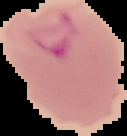
Summary:
  - Malaria status: parasitized
  - Image type: cell region segmented out of the field of view; surrounding area masked to black
  - Image size: 127×136 pixels
  - Preparation: thin blood smear